Give the position of every malaria parasite.
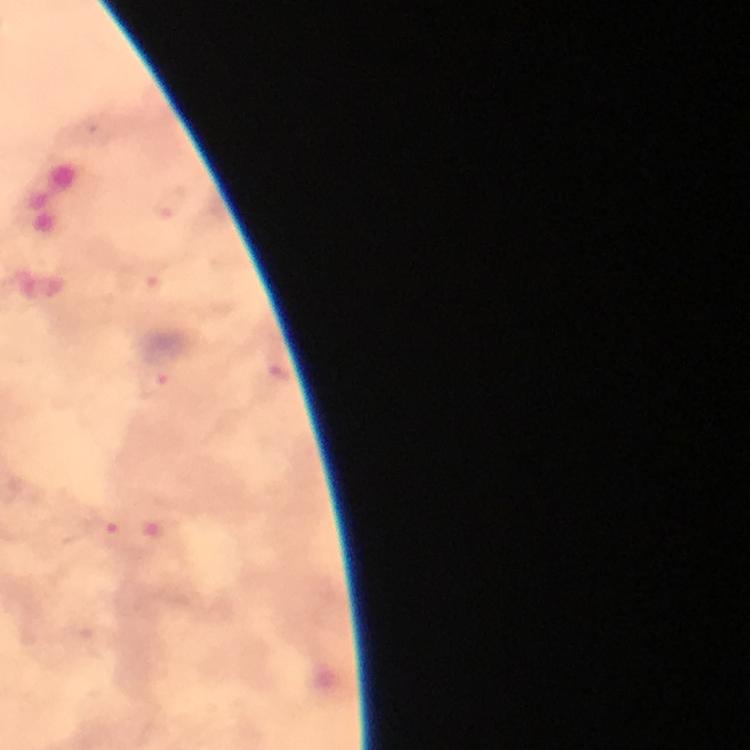
Approximate centers as [x, y] in pixels.
Malaria parasites: [155, 386], [105, 533].

stain = Giemsa
magnification = 100x
capture = smartphone mounted on the microscope
preparation = thick smear
context = from a diagnostic examination for malaria
cropped from = a single field of view
image size = 750×750 pixels
immersion oil = applied